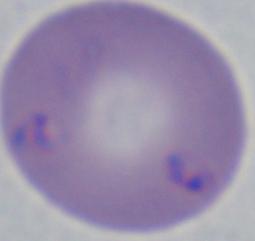
magnification = 1000x
identification = Babesia
modality = photomicrograph